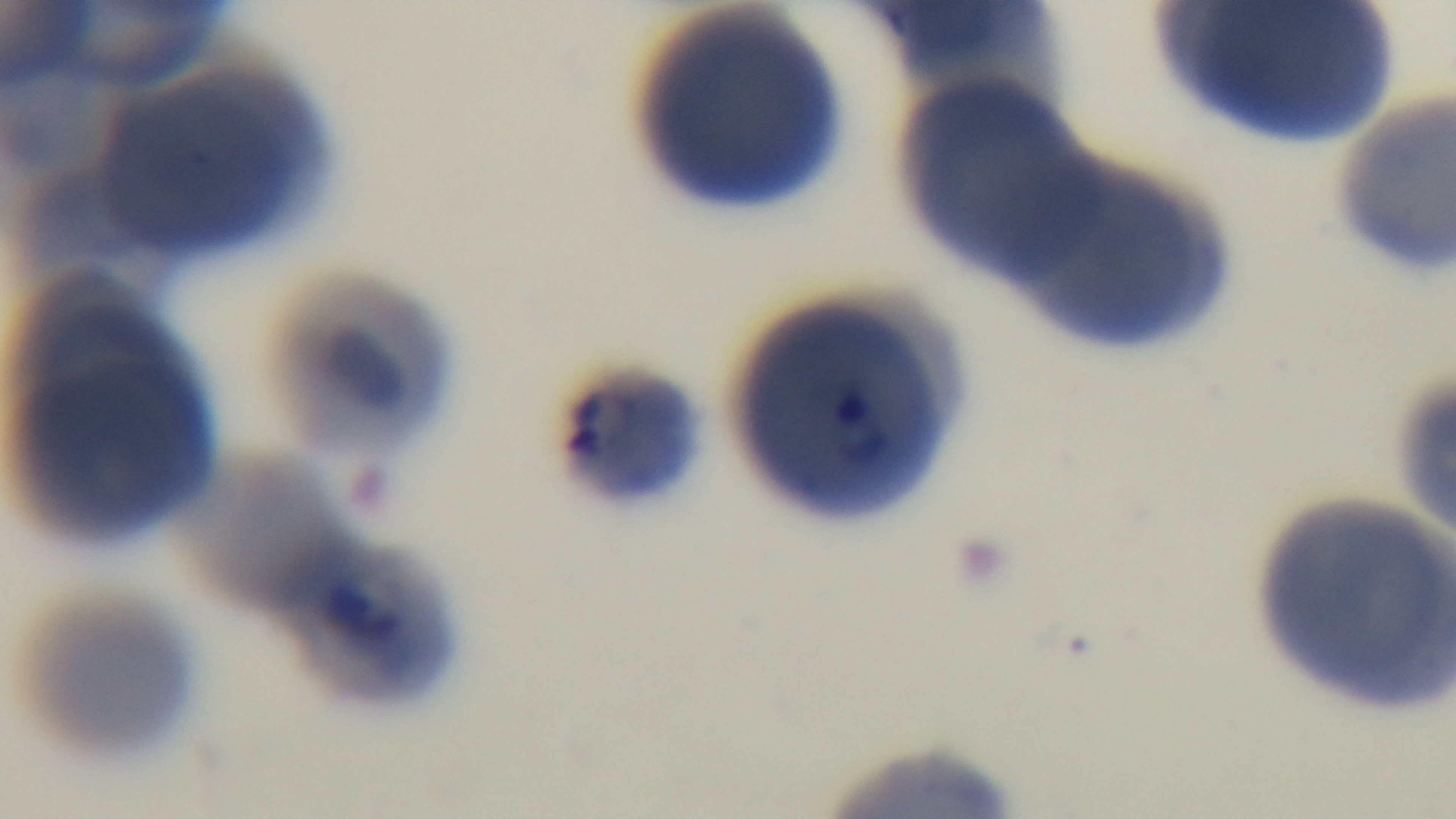
stain = Giemsa
objective = 100x oil immersion
modality = light microscopy
preparation = thin blood film
field of view = single
malaria status = positive
capture = mounted 4K digital camera